Report the malaria status of this cell.
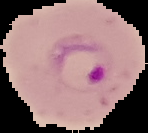

It is parasitized.

Summary:
  - Image type: segmented cell region on a black background
  - Preparation: thin blood smear
  - Image size: 148×133 pixels